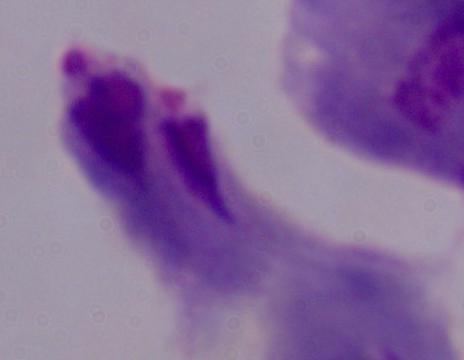
Summary:
  - Magnification: 1000x
  - Identification: trichomonad
  - Modality: photomicrograph